Evaluate for Plasmodium parasites.
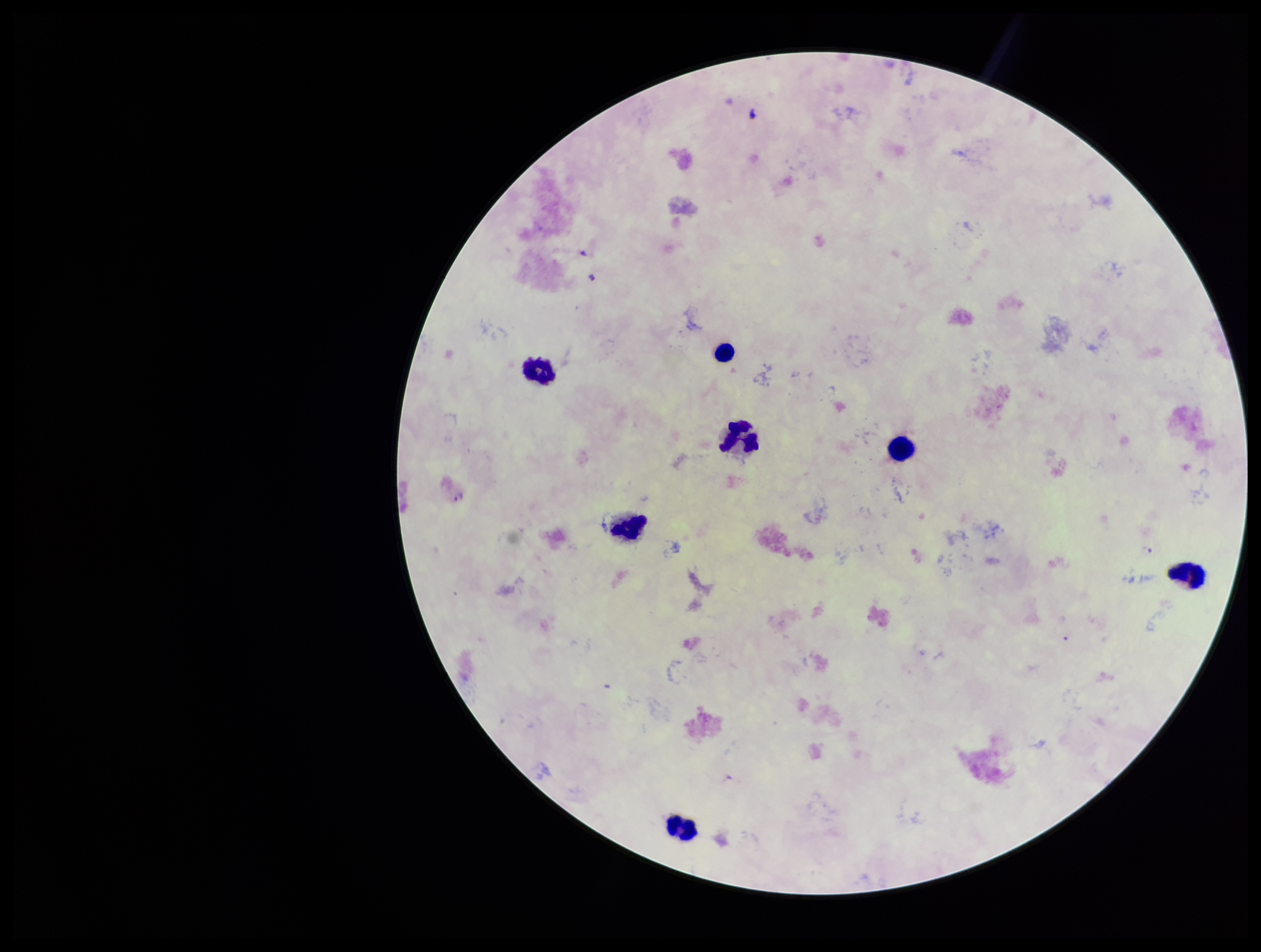

Detected.

field of view = single
preparation = thick blood smear
leukocyte count = 7
stain = Giemsa
image size = 1261×952 pixels
capture = smartphone photograph through the microscope eyepiece
parasite count = 2
patient malaria status = infected
species reported for this patient = Plasmodium falciparum